Outline each uninfected red blood cell.
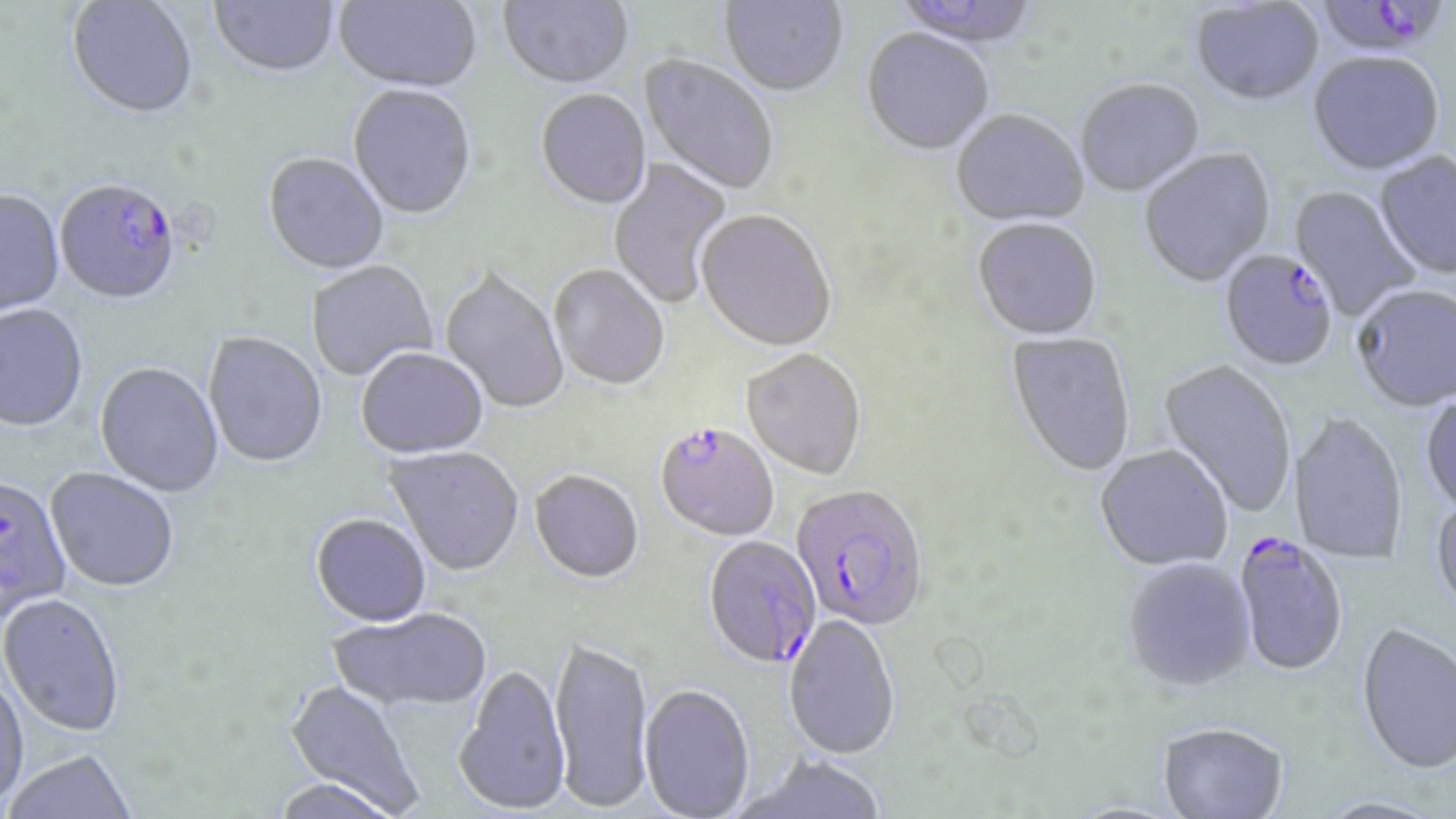
Approximate bounding boxes as (x1,y1)-(x2,y2) corner pairs in pixels.
Uninfected red blood cells: (209,0)-(339,80), (333,0)-(482,95), (499,0)-(633,92), (720,0)-(848,99), (893,0)-(1044,52), (67,1)-(199,122), (1191,1)-(1324,109), (861,30)-(994,158), (638,54)-(778,196), (1308,54)-(1445,177), (1076,81)-(1205,199), (348,86)-(477,222), (535,90)-(652,212), (951,111)-(1089,229), (1139,149)-(1276,289), (1375,153)-(1456,281), (262,154)-(389,276), (608,156)-(733,309), (1288,186)-(1420,320), (0,192)-(65,318), (695,211)-(836,353), (972,219)-(1102,342), (306,262)-(438,381), (549,266)-(669,392), (439,269)-(569,414), (1352,286)-(1456,413), (0,306)-(88,433), (1005,332)-(1136,479), (203,333)-(328,470), (356,350)-(489,460), (742,350)-(866,482), (1158,360)-(1296,518), (94,363)-(223,499), (1420,391)-(1456,520), (1288,413)-(1408,566), (1095,446)-(1233,573), (383,448)-(524,578), (44,469)-(179,594), (529,473)-(644,586), (1429,498)-(1456,621), (310,515)-(431,628), (1122,560)-(1256,694), (0,595)-(125,739), (327,609)-(493,714), (784,614)-(901,760), (1355,625)-(1456,779), (550,638)-(654,814), (453,667)-(571,817), (0,672)-(29,811), (284,680)-(422,815), (640,685)-(755,819), (1157,725)-(1288,819), (3,750)-(138,818), (738,755)-(889,818), (270,778)-(403,819), (1312,799)-(1443,819).

Summary:
  - Plasmodium falciparum-infected red blood cell locations: (1315,0)-(1448,53), (52,187)-(177,308), (1218,251)-(1338,373), (654,424)-(779,543), (0,477)-(73,625), (791,485)-(929,632), (1232,534)-(1348,680), (703,537)-(822,671)
  - Slide-level diagnosis: Plasmodium falciparum
  - Magnification: 1000x
  - Field of view: single
  - Stain: May-Grünwald-Giemsa
  - Image size: 1456×819 pixels
  - Preparation: thin blood film
  - Modality: light microscopy